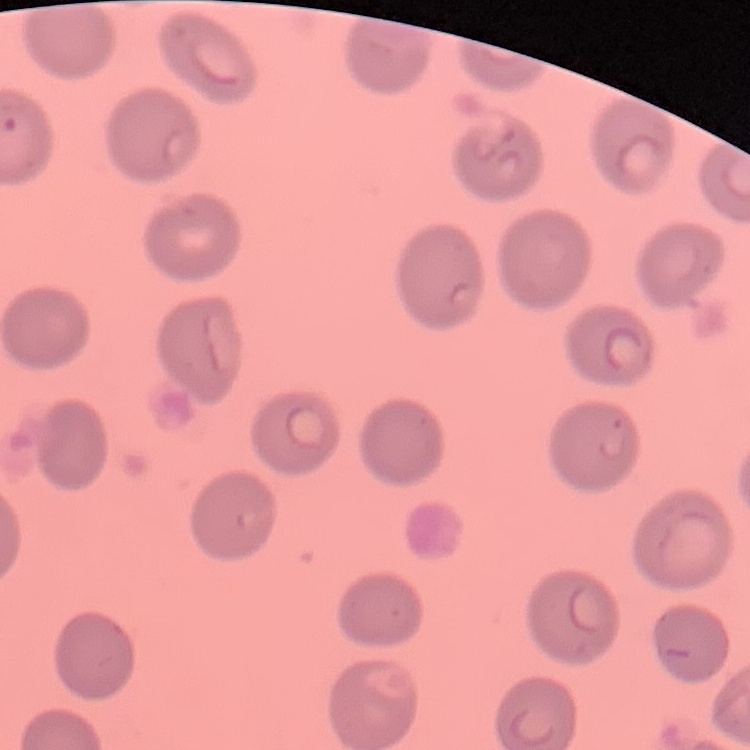
Summary:
  - Red blood cell morphology: no rouleaux formation
  - Image type: square crop of a larger photomicrograph
  - Stain: Field's or Giemsa
  - Preparation: thin blood film